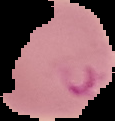

Segmented cell region on a black background. Image is 115×121 pixels. From a thin blood film. Result: Plasmodium parasites detected.